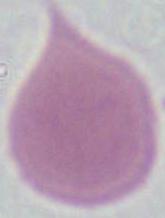
Summary:
  - Magnification: 1000x
  - Identification: erythrocyte
  - Modality: photomicrograph